Name the cell type shown.
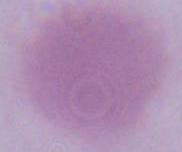

This is an erythrocyte.

Captured at 1000x magnification. Photomicrograph.